Give the extent of all uninfected red blood cells.
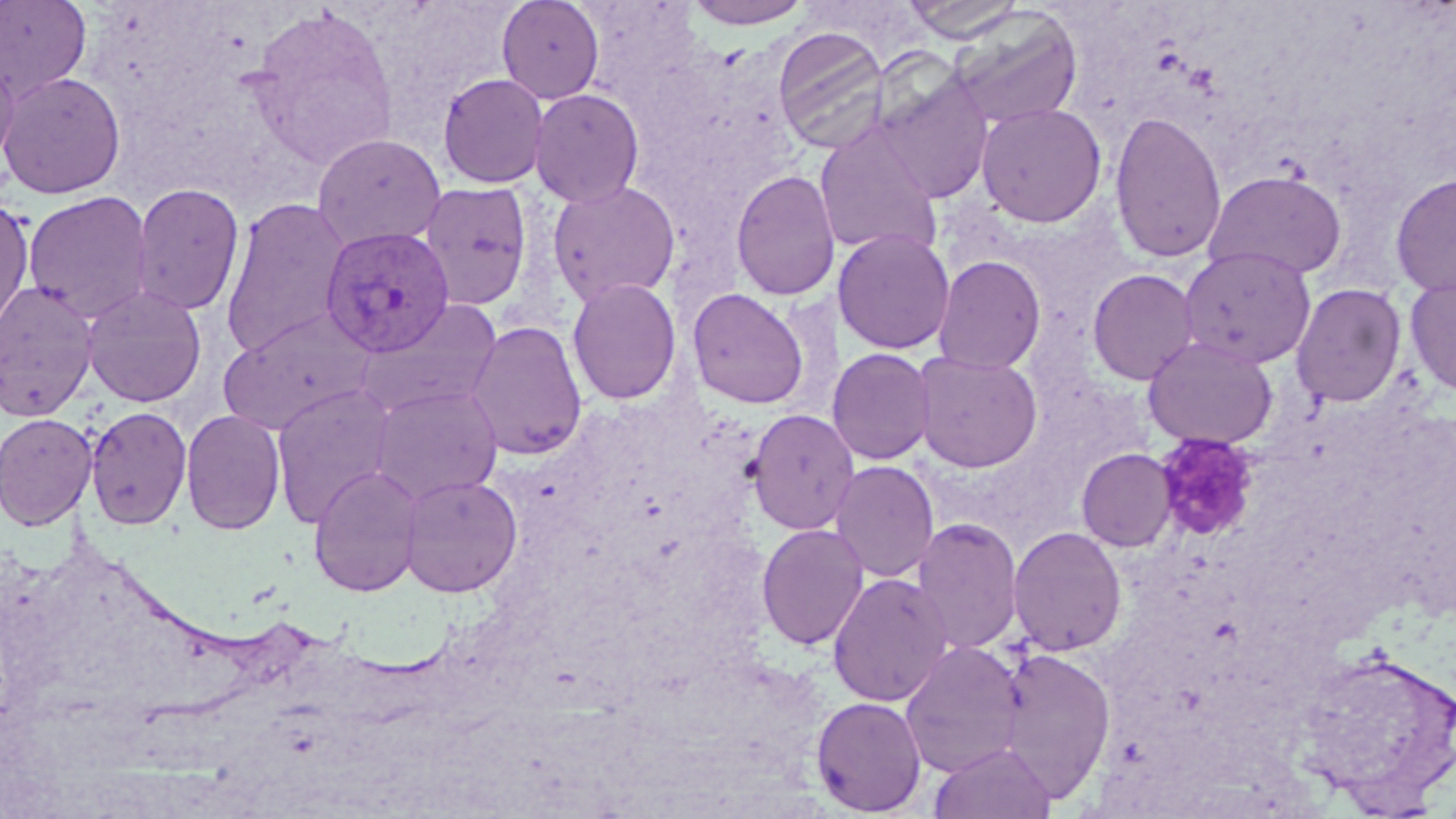
Approximate bounding boxes as (x1, y1, x2, y2) in pixels.
Uninfected red blood cells: (0, 0, 93, 103), (496, 0, 605, 104), (681, 0, 816, 29), (901, 0, 1027, 43), (244, 8, 401, 169), (947, 8, 1084, 130), (772, 25, 890, 153), (0, 49, 19, 173), (1, 71, 126, 199), (437, 72, 549, 189), (873, 73, 994, 204), (529, 88, 645, 208), (975, 102, 1107, 227), (1109, 110, 1228, 265), (813, 124, 944, 259), (312, 132, 447, 251), (731, 169, 840, 302), (1203, 170, 1346, 281), (1390, 172, 1456, 298), (547, 179, 681, 307), (418, 180, 533, 311), (131, 182, 245, 317), (22, 190, 154, 323), (0, 196, 35, 337), (219, 196, 350, 360), (832, 227, 955, 354), (1178, 245, 1316, 369), (932, 255, 1046, 374), (1087, 268, 1200, 385), (1404, 275, 1456, 396), (566, 277, 682, 406), (0, 280, 99, 421), (1291, 282, 1407, 408), (81, 285, 207, 407), (686, 287, 811, 410), (353, 299, 504, 418), (218, 309, 375, 435), (464, 320, 588, 461), (1143, 335, 1278, 449), (826, 347, 935, 466), (911, 350, 1044, 473), (271, 383, 397, 527), (368, 384, 504, 503), (85, 405, 192, 529), (745, 408, 860, 535), (180, 409, 286, 536), (0, 412, 98, 531), (1076, 448, 1177, 551), (829, 460, 940, 583), (308, 465, 425, 597), (399, 475, 523, 598), (911, 517, 1024, 655), (756, 523, 870, 651), (1008, 525, 1127, 656), (827, 572, 954, 707), (900, 640, 1026, 778), (1294, 644, 1456, 810), (996, 647, 1116, 800), (811, 696, 927, 816), (929, 743, 1056, 819).

slide-level diagnosis = Plasmodium vivax
platelet locations = approximate bounding boxes as (x1, y1, x2, y2) in pixels: (1154, 434, 1260, 543)
magnification = 1000x
field of view = one of a larger specimen
Plasmodium vivax-infected red blood cell locations = approximate bounding boxes as (x1, y1, x2, y2) in pixels: (319, 226, 455, 357)
modality = light microscopy
image size = 1456×819 pixels
stain = May-Grünwald-Giemsa
preparation = thin blood smear